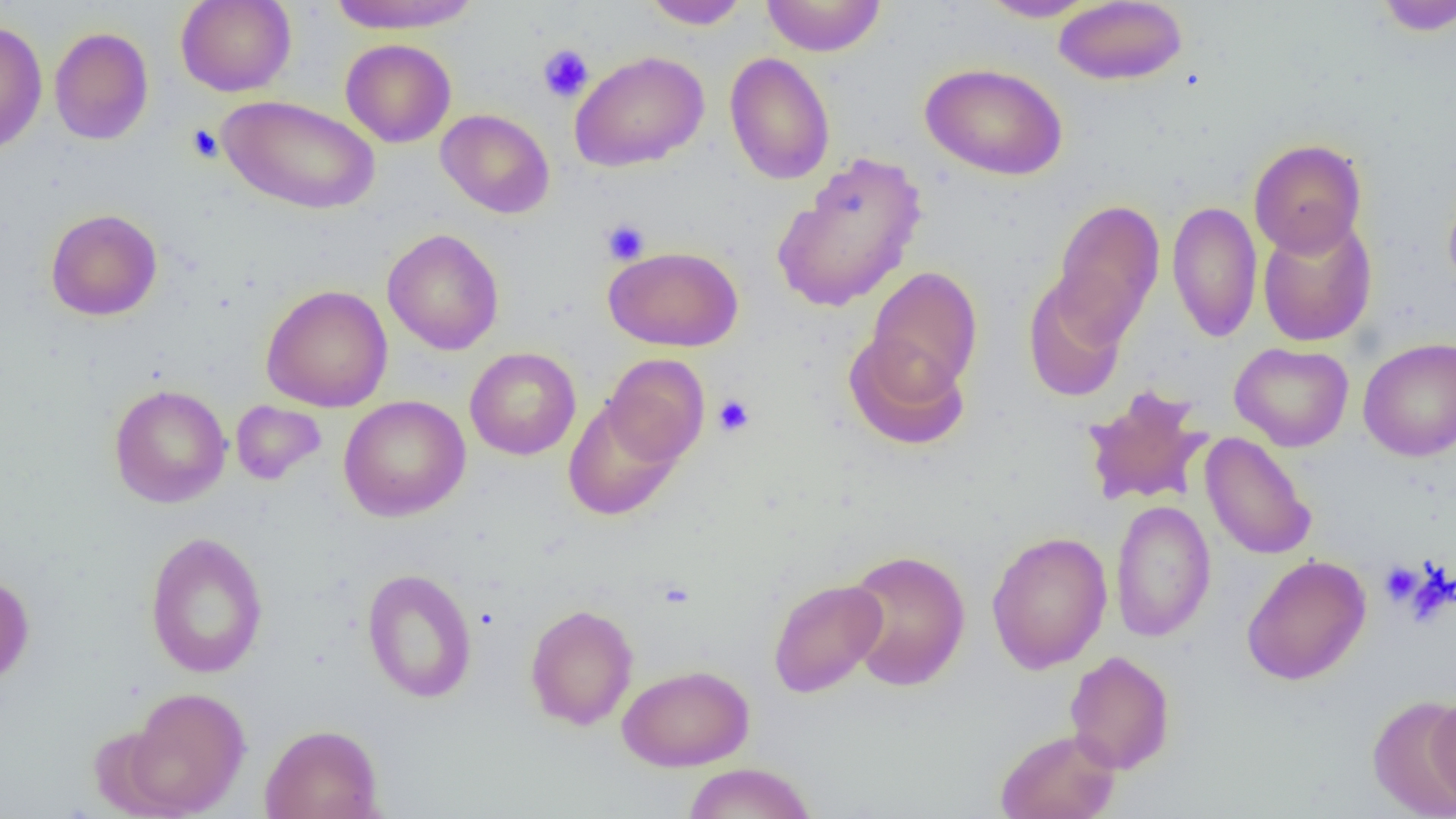
Approximate bounding boxes as (x1, y1, x2, y2) in pixels. Platelet locations: (537, 44, 594, 103), (185, 124, 224, 163), (601, 218, 651, 265), (713, 395, 755, 437), (1379, 561, 1422, 606). Uninfected red blood cell locations: (175, 0, 296, 97), (327, 0, 483, 33), (641, 0, 750, 30), (761, 0, 887, 57), (1372, 0, 1456, 36), (978, 1, 1099, 22), (1053, 1, 1188, 86), (0, 18, 48, 155), (49, 26, 154, 145), (341, 38, 456, 147), (569, 50, 709, 172), (724, 52, 836, 185), (920, 62, 1069, 181), (218, 95, 380, 215), (435, 109, 555, 218), (1249, 138, 1367, 257), (771, 151, 927, 313), (1443, 182, 1456, 301), (1050, 198, 1165, 342), (1167, 200, 1262, 343), (45, 208, 163, 321), (1257, 215, 1378, 347), (382, 228, 504, 355), (604, 245, 743, 352), (865, 266, 982, 397), (1022, 273, 1130, 404), (261, 284, 393, 413), (843, 332, 970, 451), (1358, 337, 1456, 462), (1229, 342, 1354, 452), (464, 347, 581, 461), (603, 354, 710, 467), (108, 384, 232, 508), (1080, 384, 1213, 509), (338, 395, 470, 521), (563, 398, 682, 521), (231, 400, 326, 485), (1200, 432, 1316, 561), (1110, 499, 1216, 643), (144, 531, 268, 679), (986, 531, 1113, 674), (842, 548, 971, 691), (1241, 554, 1372, 686), (360, 568, 478, 703), (0, 573, 35, 689), (767, 578, 887, 698), (524, 603, 639, 730), (1064, 650, 1176, 774), (617, 664, 755, 771), (121, 686, 251, 817), (1427, 692, 1455, 812), (1367, 695, 1456, 818), (259, 723, 383, 819), (995, 728, 1121, 819), (681, 762, 817, 819). Slide-level diagnosis: no evidence of blood parasites. One field of a larger specimen. Optical microscopy. Thin blood film. Captured at 1000x magnification. Image is 1456×819 pixels.